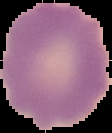
image_size: 112×133 pixels
preparation: thin blood film
image_type: cell region segmented out of the field of view; surrounding area masked to black
result: no Plasmodium parasites seen